Locate every leukocyte (white blood cell).
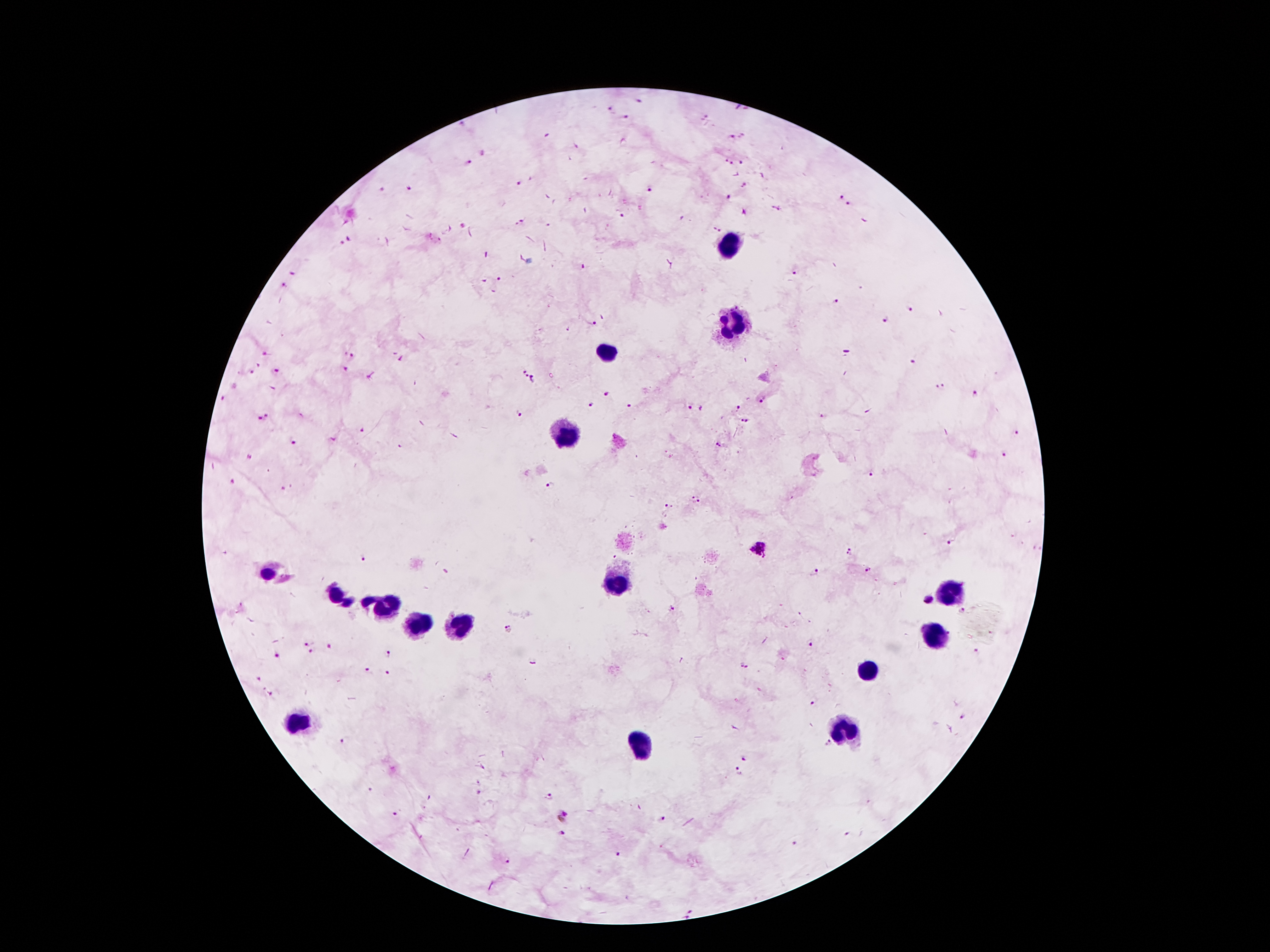
Approximate centers as {x, y} in pixels.
Leukocytes: {727, 245}, {733, 324}, {605, 350}, {566, 434}, {618, 585}, {950, 593}, {387, 606}, {419, 625}, {463, 627}, {931, 637}, {866, 672}, {299, 723}, {843, 731}, {641, 744}.

Summary:
  - Plasmodium parasite locations: {612, 110}, {626, 118}, {730, 135}, {467, 161}, {729, 162}, {743, 163}, {519, 184}, {408, 187}, {651, 188}, {839, 196}, {730, 199}, {849, 206}, {621, 217}, {520, 222}, {716, 230}, {342, 245}, {796, 272}, {292, 273}, {498, 278}, {284, 285}, {836, 301}, {909, 310}, {885, 321}, {593, 323}, {265, 354}, {349, 354}, {913, 363}, {345, 370}, {275, 371}, {521, 371}, {252, 373}, {536, 380}, {940, 386}, {607, 394}, {977, 394}, {223, 399}, {761, 399}, {590, 405}, {689, 407}, {629, 408}, {737, 408}, {520, 415}, {825, 416}, {264, 417}, {744, 419}, {364, 431}, {1016, 433}, {292, 443}, {718, 444}, {1005, 453}, {250, 456}, {871, 474}, {234, 482}, {550, 485}, {283, 488}, {694, 499}, {670, 504}, {950, 543}, {758, 550}, {849, 552}, {363, 559}, {869, 571}, {815, 573}, {930, 599}, {671, 607}, {962, 611}, {508, 627}, {309, 640}, {811, 644}, {330, 648}, {312, 653}, {976, 653}, {389, 655}, {277, 657}, {533, 661}, {744, 666}, {366, 671}, {390, 671}, {257, 679}, {271, 693}, {814, 700}, {963, 716}, {344, 740}, {827, 743}, {746, 755}, {738, 771}, {369, 791}, {479, 793}, {549, 796}, {394, 812}, {563, 815}, {662, 819}, {561, 833}, {847, 834}, {796, 844}, {620, 855}, {507, 861}, {691, 912}
  - Patient malaria status: infected with Plasmodium falciparum
  - Capture: smartphone through the microscope eyepiece
  - Magnification: 100x
  - Stain: Giemsa
  - Field of view: single
  - Preparation: thick blood film
  - Image size: 1270×952 pixels